Locate every uninfected red blood cell.
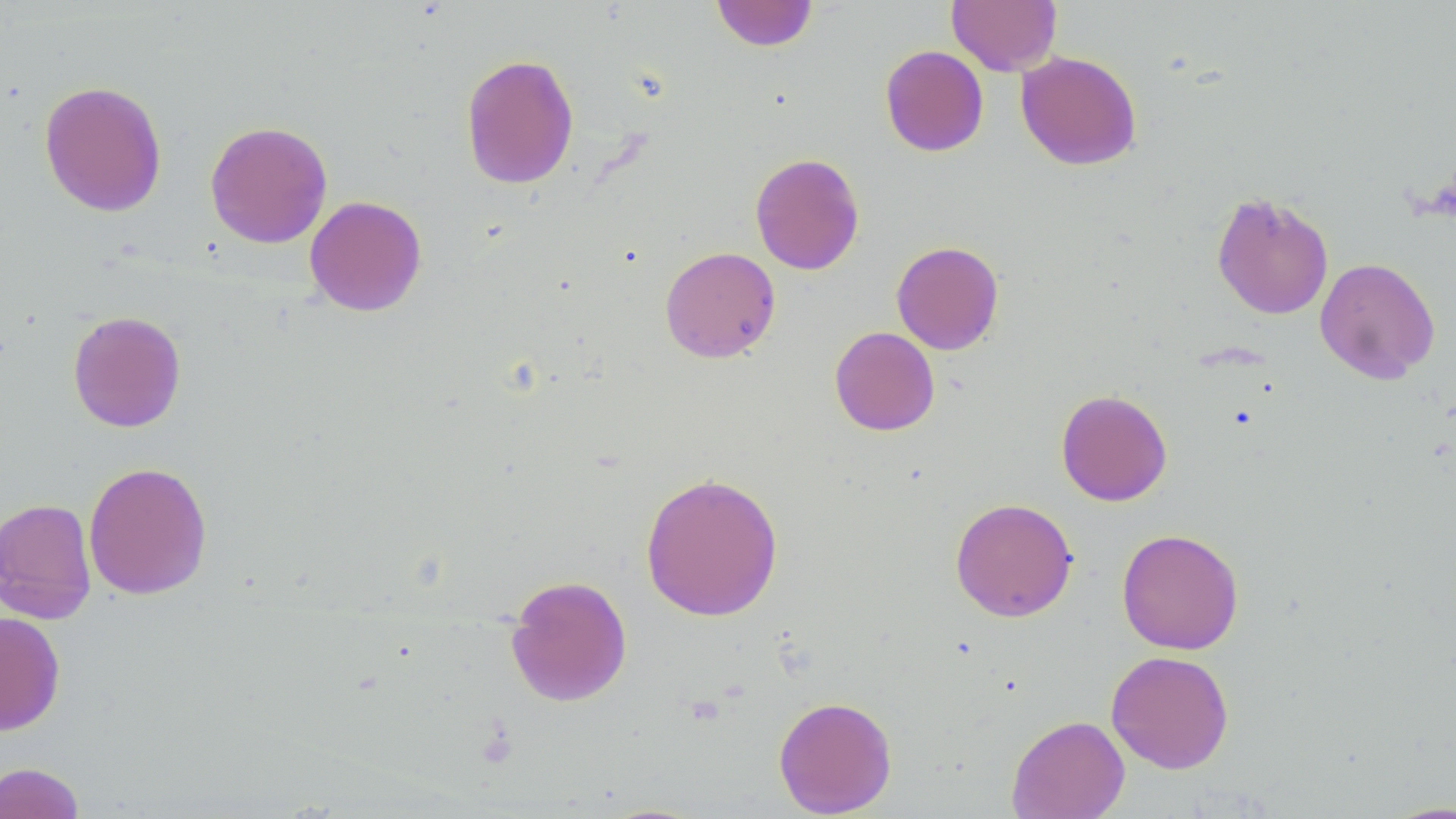
Approximate bounding boxes as (x1,y1)-(x2,y2) corner pairs in pixels.
Uninfected red blood cells: (947,0)-(1062,75), (711,1)-(819,51), (880,45)-(989,156), (1016,51)-(1142,171), (460,53)-(579,190), (39,80)-(167,218), (205,120)-(333,249), (749,152)-(865,275), (1211,189)-(1334,321), (304,195)-(427,316), (891,241)-(1004,355), (659,246)-(780,363), (1315,257)-(1440,384), (67,310)-(186,432), (829,326)-(940,436), (1055,389)-(1173,506), (83,461)-(213,600), (640,471)-(784,622), (0,498)-(97,624), (950,498)-(1078,622), (1116,527)-(1244,655), (505,574)-(633,707), (0,611)-(66,735), (1106,650)-(1234,774), (773,696)-(897,817), (1006,714)-(1130,819), (0,761)-(85,819).

Summary:
  - Slide-level diagnosis: negative for blood parasites
  - Modality: light microscopy
  - Magnification: 1000x
  - Field of view: one of a larger specimen
  - Image size: 1456×819 pixels
  - Preparation: thin blood film
  - Stain: May-Grünwald-Giemsa